Locate every blood parasite and identify its species.
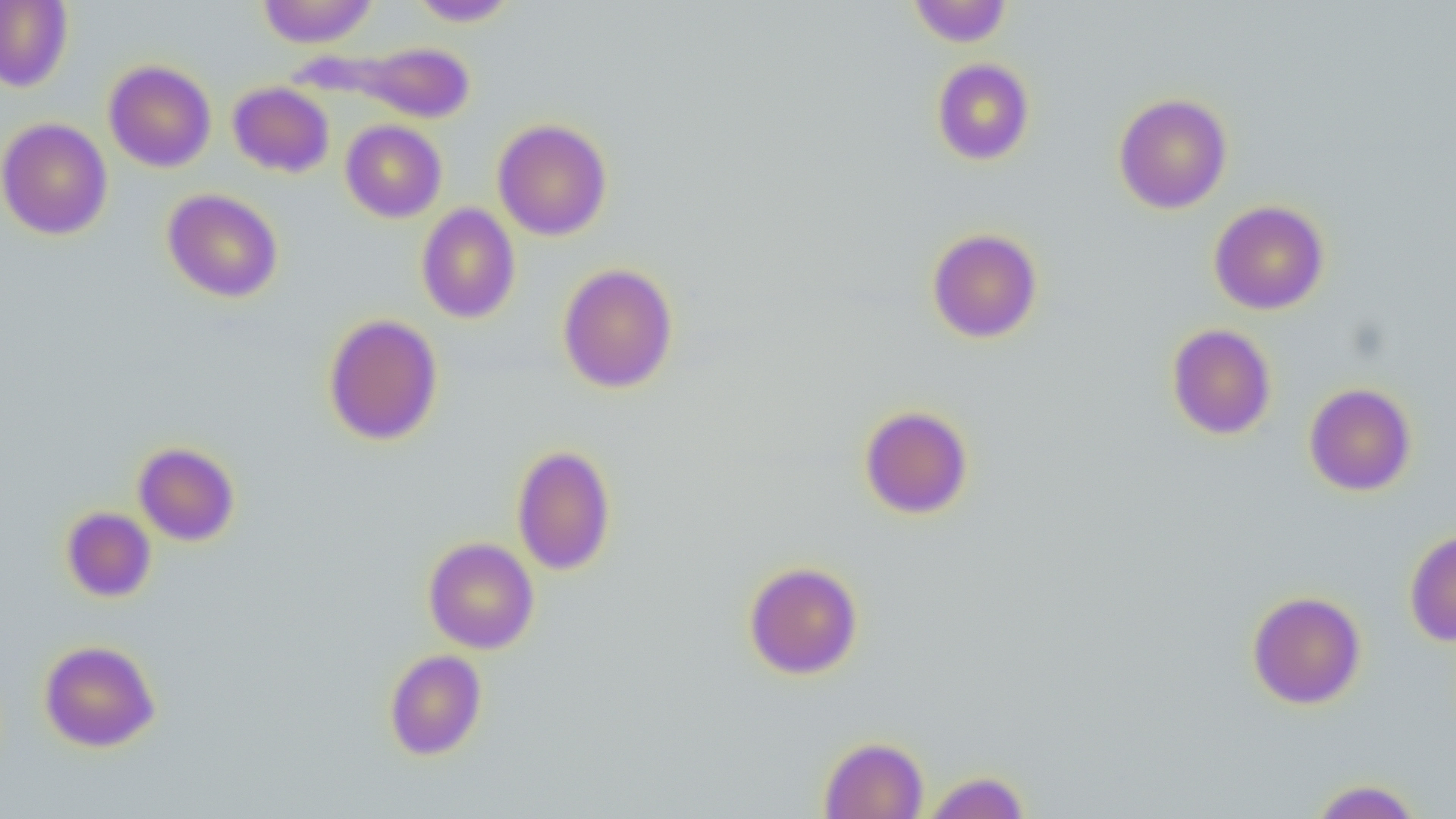

No blood parasites observed.

slide_level_diagnosis: no evidence of blood parasites
image_size: 1456×819 pixels
modality: light microscopy
uninfected_red_blood_cell_locations: 'approximate bounding boxes as [x1, y1, x2, y2] in pixels: [256, 0, 380, 48], [407, 0, 519, 26], [908, 0, 1012, 47], [0, 1, 73, 92], [337, 42, 476, 123], [931, 58, 1035, 165], [104, 60, 216, 172], [228, 81, 335, 177], [1113, 93, 1233, 214], [0, 117, 113, 240], [492, 119, 612, 241], [340, 120, 447, 223], [162, 188, 283, 302], [1209, 200, 1329, 315], [416, 203, 520, 323], [927, 228, 1043, 343], [558, 263, 678, 393], [323, 313, 444, 445], [1166, 323, 1277, 440], [1303, 382, 1417, 496], [859, 406, 974, 519], [133, 442, 240, 546], [512, 444, 617, 576], [61, 506, 156, 603], [1404, 529, 1456, 646], [424, 537, 539, 654], [744, 561, 863, 679], [1247, 590, 1366, 709], [39, 640, 160, 753], [384, 650, 488, 760], [818, 736, 929, 818], [921, 770, 1032, 819], [1308, 779, 1423, 818]'
field_of_view: one of a larger specimen
magnification: 1000x
preparation: thin blood smear